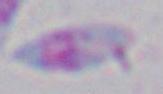
magnification = 1000x
identification = Toxoplasma gondii
modality = photomicrograph